Point out each Plasmodium parasite and each leukocyte.
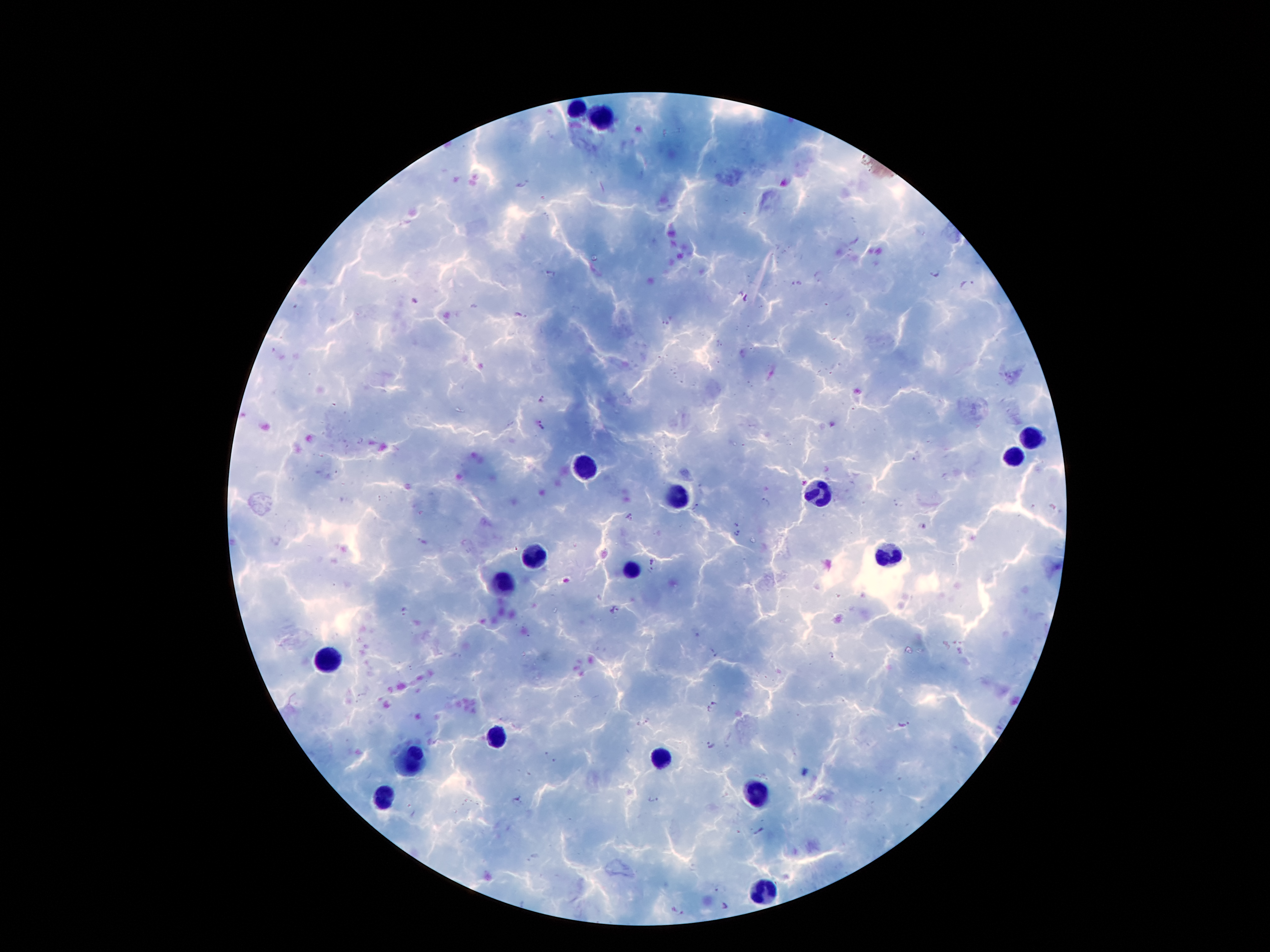
Approximate centers as {x, y} in pixels.
Plasmodium parasites: {523, 183}, {552, 274}, {935, 275}, {818, 277}, {797, 284}, {967, 285}, {748, 299}, {416, 301}, {520, 315}, {665, 323}, {542, 400}, {541, 426}, {917, 456}, {767, 502}, {897, 504}, {698, 507}, {631, 516}, {921, 526}, {739, 534}, {422, 542}, {653, 565}, {613, 609}, {404, 613}, {711, 653}, {831, 657}, {363, 697}, {712, 705}, {642, 722}, {902, 724}, {709, 746}, {546, 753}, {556, 761}, {651, 798}, {519, 800}, {760, 831}, {532, 858}, {726, 907}, {677, 913}.
Leukocytes: {577, 109}, {608, 121}, {1026, 439}, {1013, 454}, {584, 466}, {813, 493}, {674, 498}, {534, 555}, {888, 555}, {631, 572}, {506, 586}, {331, 661}, {497, 738}, {409, 757}, {658, 757}, {754, 793}, {379, 802}, {767, 891}.

Summary:
  - Patient malaria status: infected with Plasmodium falciparum
  - Image size: 1270×952 pixels
  - Stain: Giemsa
  - Preparation: thick blood film
  - Field of view: one from this slide
  - Magnification: 100x
  - Capture: smartphone camera through the microscope eyepiece